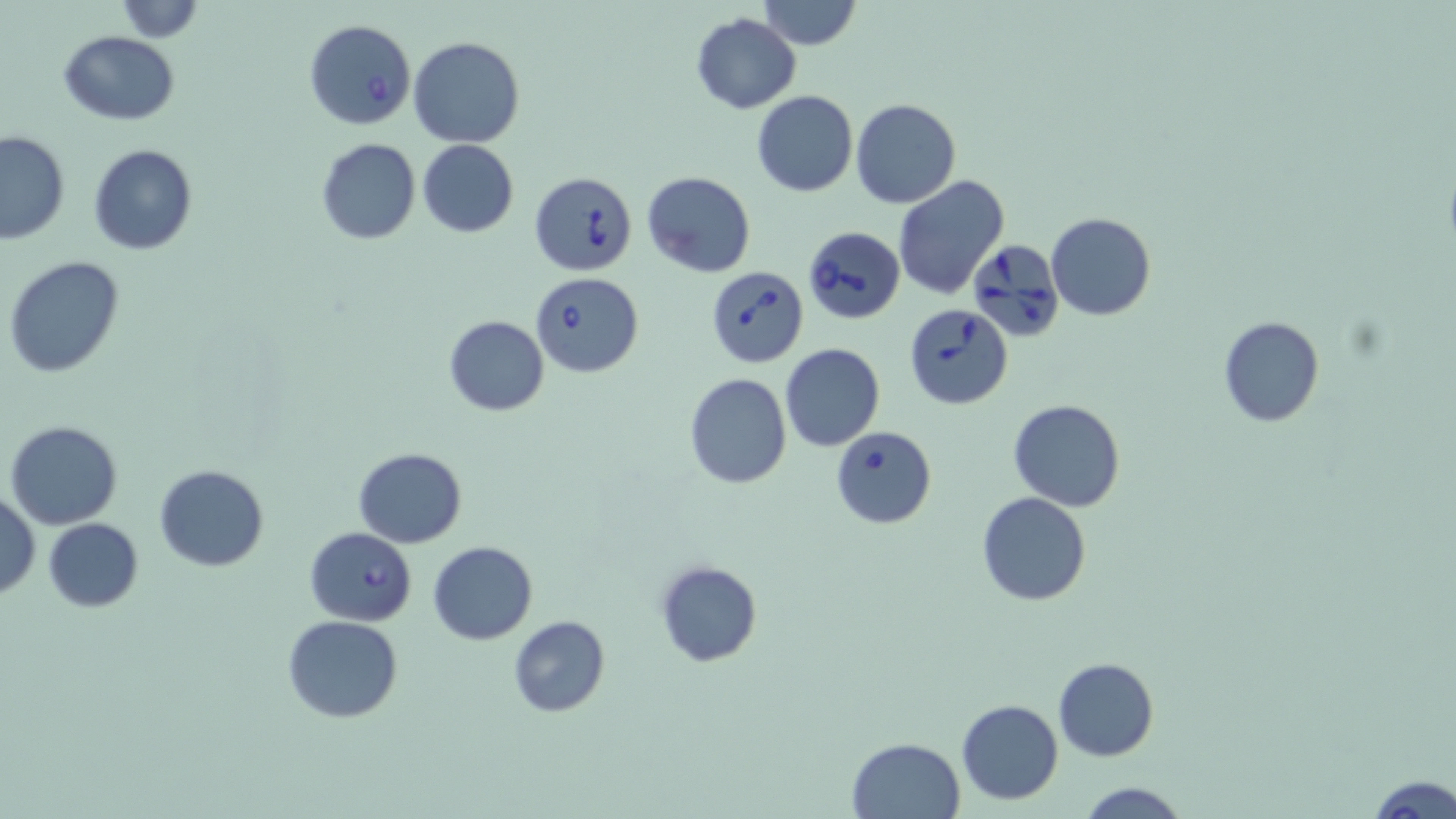

Approximate bounding boxes as [x1, y1, x2, y2] in pixels. Uninfected red blood cell locations: [112, 0, 206, 41], [759, 0, 861, 51], [691, 12, 801, 113], [59, 31, 181, 124], [408, 35, 525, 147], [752, 90, 858, 196], [850, 98, 961, 208], [0, 130, 70, 243], [315, 138, 422, 245], [418, 140, 518, 237], [87, 143, 198, 255], [642, 171, 756, 276], [893, 175, 1010, 300], [1046, 213, 1156, 322], [3, 255, 124, 379], [443, 315, 550, 417], [1218, 316, 1324, 427], [780, 343, 886, 452], [684, 374, 791, 490], [1007, 397, 1127, 510], [4, 419, 123, 530], [353, 448, 468, 547], [154, 464, 269, 571], [1, 489, 40, 599], [977, 492, 1091, 606], [43, 518, 144, 612], [428, 540, 538, 644], [655, 560, 762, 668], [283, 615, 405, 723], [507, 616, 610, 717], [1053, 657, 1159, 761], [956, 699, 1065, 804], [845, 738, 966, 819], [1367, 776, 1456, 817], [1076, 780, 1188, 817]. Babesia divergens-infected red blood cell locations: [303, 20, 416, 131], [529, 172, 638, 275], [803, 226, 904, 325], [968, 237, 1065, 341], [705, 266, 809, 368], [529, 270, 644, 377], [904, 305, 1014, 409], [830, 426, 937, 528], [304, 527, 417, 626]. Slide-level diagnosis: Babesia divergens. May-Grünwald-Giemsa stain. Light microscopy. One field of a larger specimen. Image is 1456×819 pixels. Thin blood smear. 1000x magnification.